Classify this cell by malaria status.
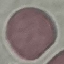

Uninfected.

Summary:
  - Image type: cell patch, automatically extracted from a larger field of view and resized to 64 × 64 pixels
  - Capture: smartphone through the microscope eyepiece
  - Stain: Giemsa
  - Preparation: thin blood film